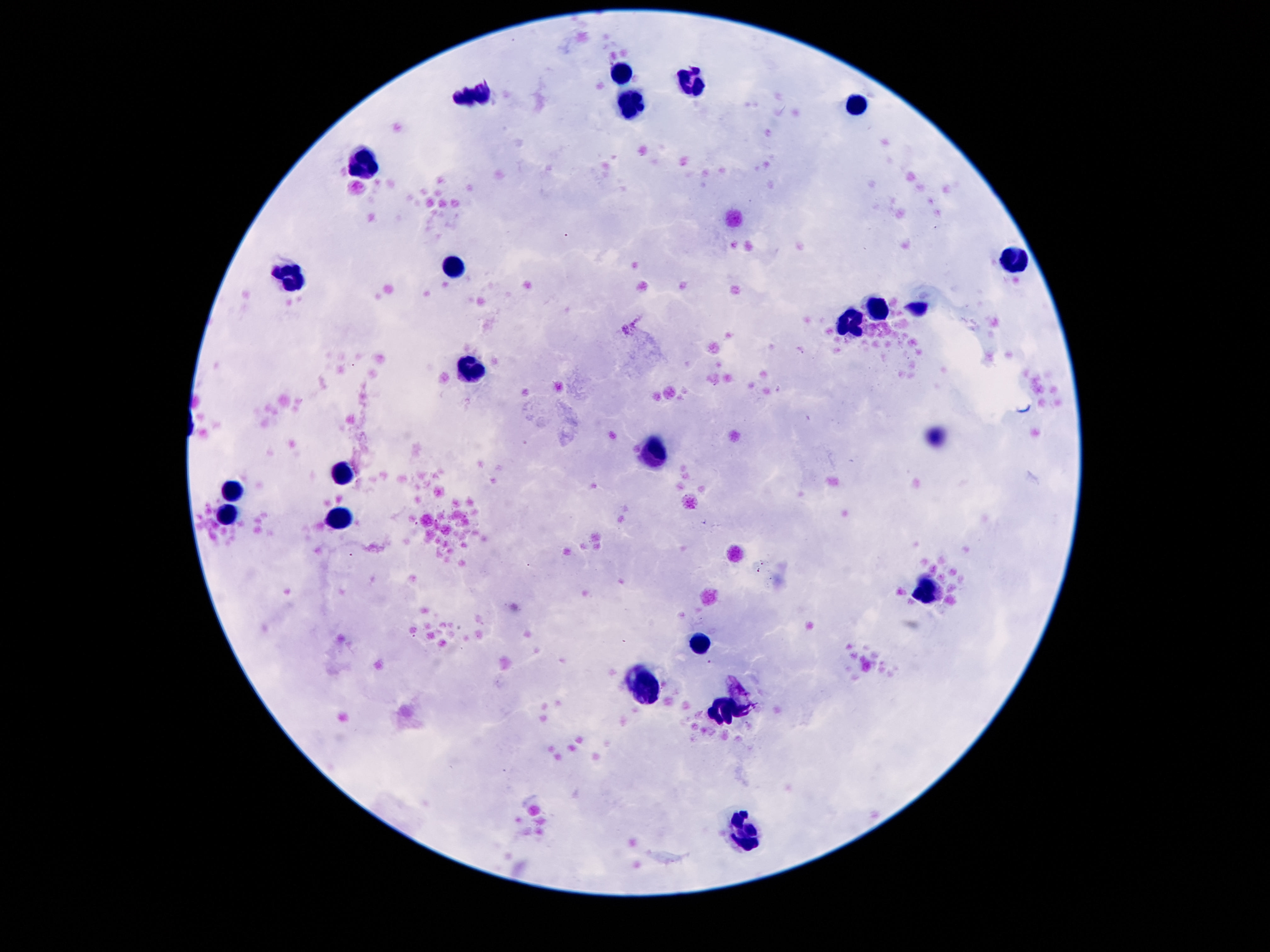

Approximate object centers, in pixels from the top-left corner. Leukocyte locations: (x=622, y=73), (x=691, y=80), (x=474, y=93), (x=859, y=104), (x=629, y=105), (x=361, y=162), (x=1014, y=259), (x=454, y=266), (x=288, y=277), (x=877, y=306), (x=852, y=321), (x=472, y=371), (x=655, y=454), (x=339, y=472), (x=233, y=489), (x=229, y=514), (x=337, y=519), (x=925, y=591), (x=697, y=644), (x=644, y=686), (x=722, y=712), (x=748, y=833). Thick blood smear. Image is 1270×952 pixels. Patient malaria status: not infected. 100x magnification. Photographed through the microscope eyepiece with a smartphone camera. Giemsa stain. Single field of view.